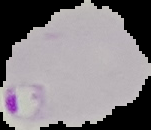

image type = segmented cell region with the area outside set to black
malaria status = parasitized
preparation = thin blood film
image size = 151×130 pixels